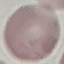

Summary:
  - Result: no malaria parasites detected
  - Capture: smartphone through the microscope eyepiece
  - Image type: cell patch, automatically extracted from a larger field of view and resized to 64 × 64 pixels
  - Preparation: thin smear
  - Stain: Giemsa